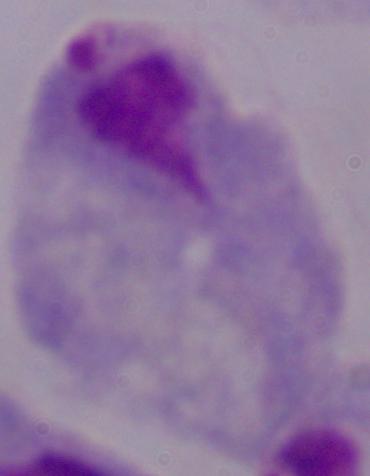

magnification: 1000x
modality: photomicrograph
identification: trichomonad